Identify the cell.
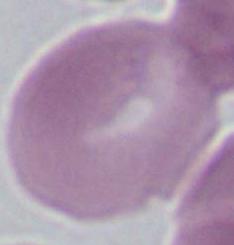

This is an erythrocyte.

Captured at 1000x magnification. Micrograph.